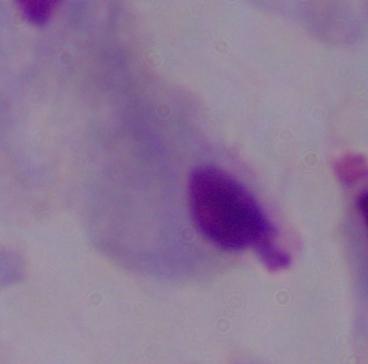

{
  "magnification": "1000x",
  "identification": "trichomonad",
  "modality": "photomicrograph"
}